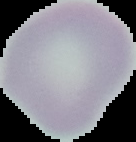
image size = 136×142 pixels
result = no Plasmodium parasites detected
image type = segmented cell region on a black background
preparation = thin blood smear